Comment on the morphology of the erythrocytes.
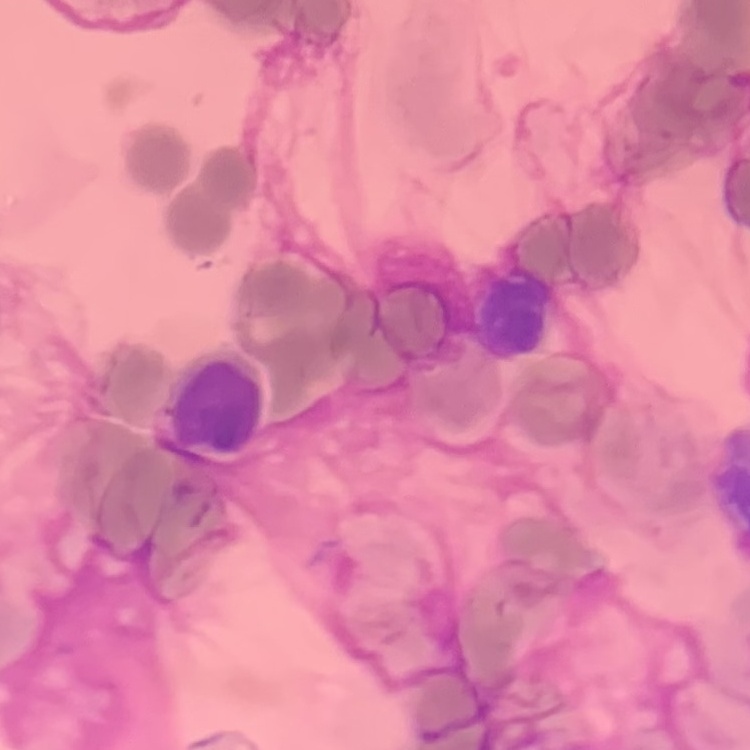
They show rouleaux formation.

stain = Field's or Giemsa
image type = square crop of a larger photomicrograph
preparation = thin blood smear